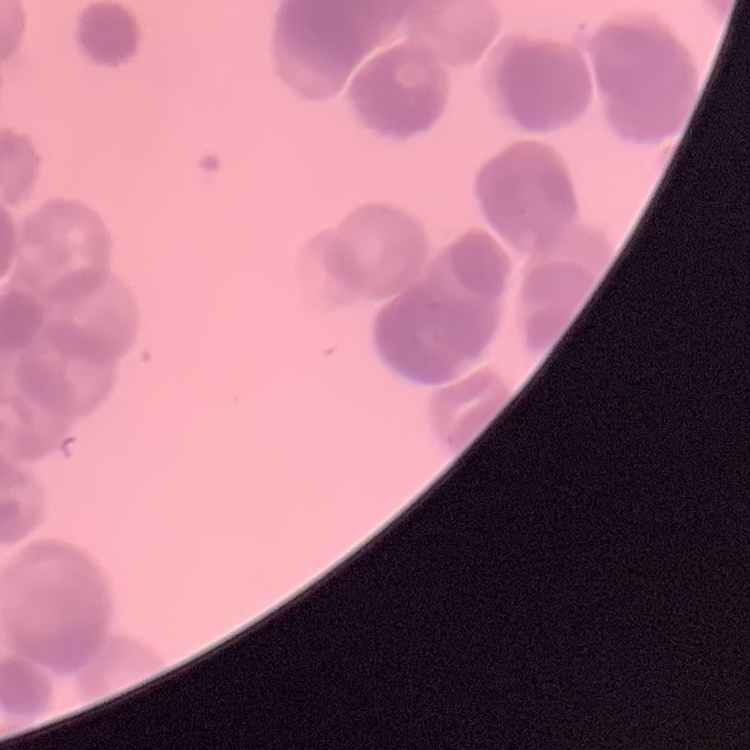
red blood cell morphology = rouleaux formation
image type = square crop of a larger photomicrograph
preparation = thin blood smear
stain = Field's or Giemsa